Describe the morphology of the red blood cells.
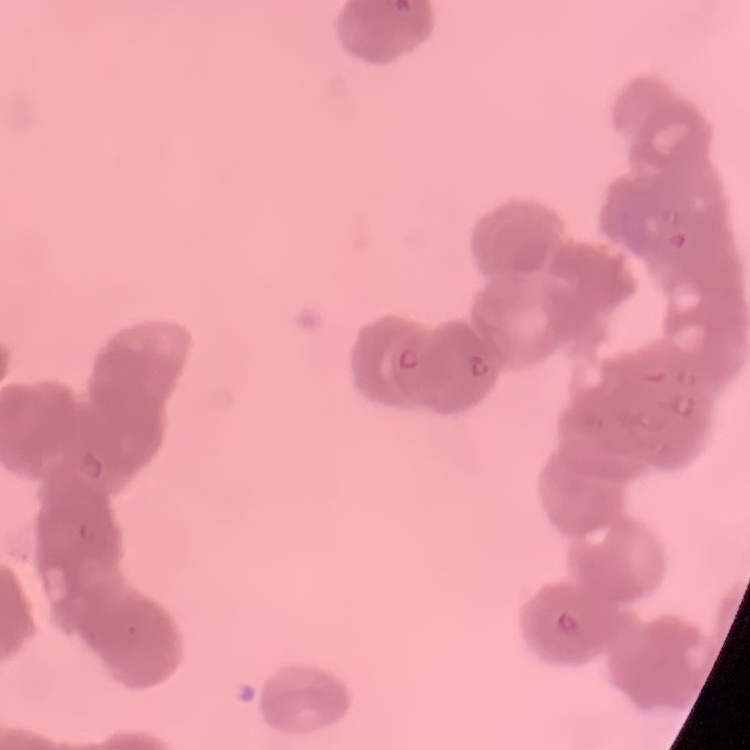
Rouleaux formation.

Field's or Giemsa stain. Thin blood film. One tile cut from a larger photomicrograph.